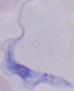

A trypanosome is seen. 1000x magnification. Micrograph.